Locate every blood parasite and identify its species.
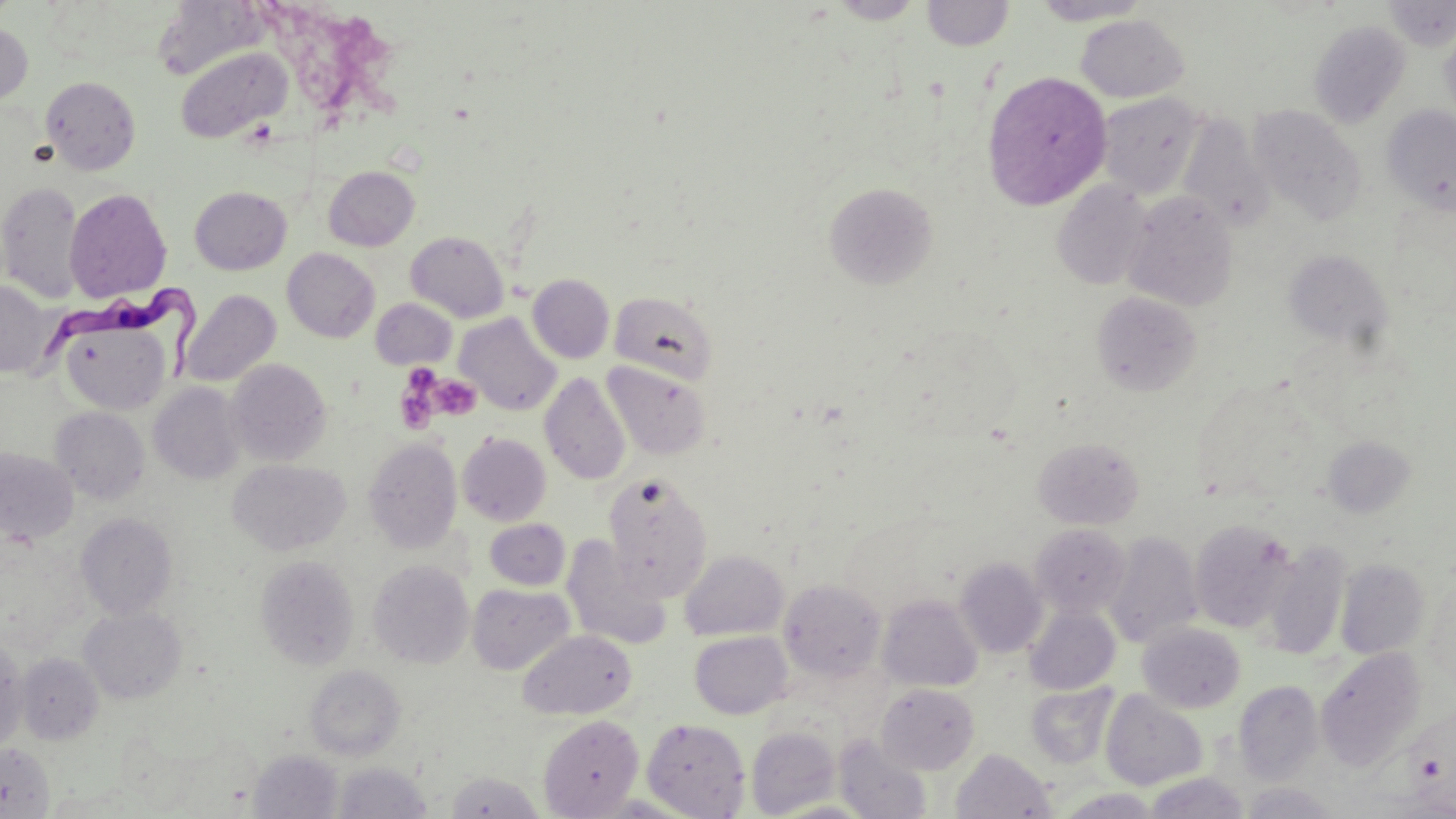

Approximate bounding boxes as (x1, y1, x2, y2) in pixels.
Trypanosoma brucei: (39, 279, 200, 387).
No Plasmodium falciparum, Plasmodium ovale, Plasmodium malariae, Plasmodium vivax, or Babesia divergens observed.

Uninfected red blood cell locations: (828, 0, 925, 23), (922, 0, 1015, 50), (1028, 0, 1153, 25), (1382, 0, 1456, 50), (153, 1, 267, 81), (1075, 14, 1190, 102), (1439, 17, 1456, 128), (1308, 19, 1411, 128), (0, 23, 33, 105), (174, 46, 292, 142), (982, 71, 1112, 210), (41, 75, 141, 175), (1096, 93, 1205, 198), (1248, 105, 1367, 224), (1382, 105, 1456, 217), (1177, 114, 1274, 233), (323, 166, 420, 251), (0, 180, 85, 303), (1051, 180, 1153, 290), (823, 182, 938, 289), (189, 186, 291, 274), (65, 188, 171, 302), (1122, 191, 1238, 312), (405, 231, 509, 322), (282, 248, 380, 342), (1283, 249, 1394, 350), (527, 274, 615, 363), (0, 280, 56, 378), (179, 289, 281, 387), (609, 289, 720, 385), (1091, 291, 1202, 397), (370, 298, 457, 369), (455, 313, 561, 415), (59, 316, 173, 415), (226, 358, 331, 466), (603, 361, 712, 460), (540, 372, 631, 485), (149, 382, 245, 484), (50, 407, 150, 503), (457, 432, 551, 526), (363, 436, 462, 553), (1033, 436, 1144, 529), (1322, 436, 1415, 518), (0, 448, 78, 544), (228, 458, 351, 556), (603, 472, 713, 599), (76, 512, 178, 619), (484, 517, 571, 590), (1189, 519, 1297, 633), (1031, 523, 1131, 618), (1104, 531, 1203, 649), (561, 534, 672, 650), (1260, 541, 1350, 660), (680, 550, 788, 641), (255, 554, 360, 670), (955, 558, 1048, 658), (1335, 558, 1431, 659), (368, 560, 475, 668), (778, 579, 886, 682), (1424, 581, 1455, 690), (467, 582, 575, 675), (877, 594, 983, 692), (1025, 606, 1120, 694), (79, 607, 186, 704), (1138, 622, 1245, 713), (518, 629, 636, 719), (689, 631, 792, 719), (1, 643, 28, 753), (1314, 648, 1425, 770), (17, 653, 103, 744), (304, 664, 405, 761), (1234, 679, 1324, 783), (1025, 682, 1119, 770), (877, 683, 980, 773), (1100, 690, 1208, 790), (538, 715, 643, 818), (640, 717, 751, 818), (745, 725, 841, 818), (834, 735, 931, 819), (0, 743, 56, 818), (951, 748, 1056, 818), (248, 750, 344, 819), (332, 761, 433, 819), (444, 771, 546, 818), (1144, 772, 1250, 818), (1237, 782, 1342, 818), (1054, 788, 1164, 818). Platelet locations: (394, 369, 442, 436), (431, 374, 480, 420). Slide-level diagnosis: Trypanosoma brucei. Optical microscopy. Captured at 1000x magnification. Image is 1456×819 pixels. Thin blood smear. May-Grünwald-Giemsa-stained preparation. Single field of view.